Which red blood cells are P. falciparum-infected, and which are of indeterminate infection status?
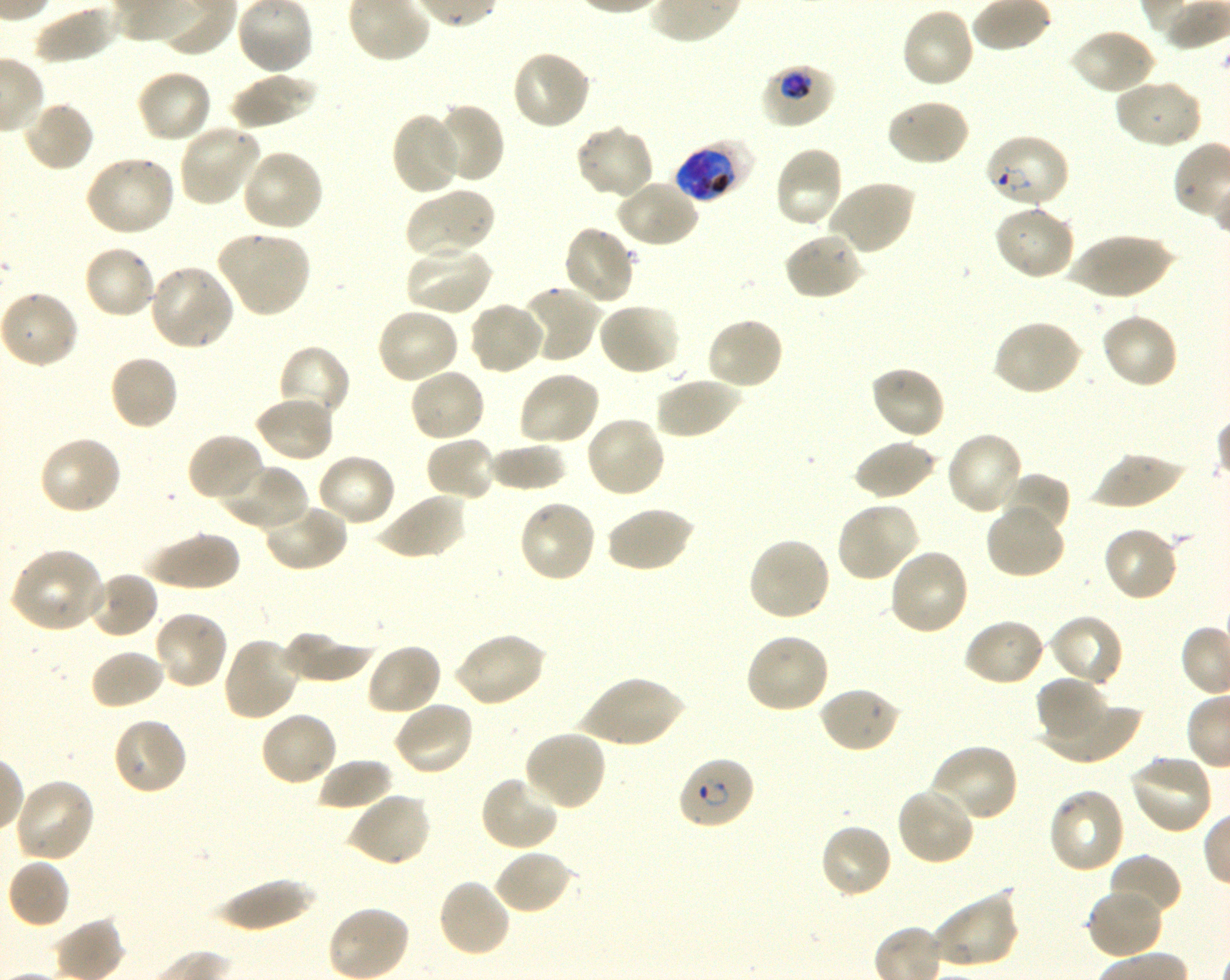
Approximate bounding boxes as [x1, y1, x2, y2] in pixels. Not every red blood cell is marked. A life-cycle stage — or a range of stages, where the recorded stages span more than one — follows each staged infected red blood cell.
Infected red blood cells: [760, 63, 837, 128] trophozoite; [984, 133, 1071, 210] ring; [675, 139, 755, 203] early trophozoite to early schizont; [678, 756, 756, 830] ring.
No red blood cells of indeterminate infection status observed.

Summary:
  - Locations of uninfected red blood cells: [33, 2, 117, 64], [900, 6, 975, 90], [1069, 27, 1157, 97], [510, 50, 593, 131], [136, 68, 214, 144], [227, 72, 319, 129], [1112, 77, 1203, 149], [885, 97, 970, 168], [22, 99, 95, 174], [429, 103, 505, 185], [391, 111, 464, 196], [177, 123, 263, 207], [575, 125, 654, 200], [773, 147, 844, 229], [240, 149, 325, 233], [85, 154, 177, 237], [615, 178, 700, 249], [826, 180, 915, 256], [403, 189, 494, 259], [993, 203, 1075, 281], [562, 224, 636, 307], [215, 230, 311, 318], [782, 230, 864, 301], [1063, 233, 1176, 300], [83, 244, 158, 319], [404, 244, 493, 317], [147, 263, 236, 351], [518, 285, 602, 364], [1, 290, 81, 369], [466, 300, 546, 376], [597, 301, 681, 376], [375, 308, 460, 385], [1100, 311, 1181, 389], [706, 317, 785, 392], [992, 318, 1083, 397], [277, 344, 352, 422], [108, 353, 179, 432], [868, 365, 946, 441], [407, 367, 487, 444], [517, 369, 601, 446], [655, 375, 743, 440], [253, 396, 335, 464], [584, 415, 667, 498], [945, 431, 1025, 517], [186, 432, 265, 504], [38, 434, 123, 515], [424, 435, 498, 503], [854, 439, 937, 501], [488, 441, 567, 492], [315, 452, 397, 528], [1089, 452, 1185, 509], [217, 461, 309, 532], [1000, 471, 1072, 535], [375, 493, 467, 561], [517, 498, 598, 584], [836, 501, 920, 583], [985, 501, 1066, 581], [261, 502, 348, 573], [605, 505, 695, 574], [1102, 525, 1181, 602], [142, 530, 242, 591], [746, 537, 831, 622], [888, 547, 971, 636], [8, 548, 110, 634], [88, 570, 160, 639], [153, 609, 231, 691], [1048, 613, 1125, 689], [962, 617, 1045, 687], [278, 629, 375, 683], [452, 631, 548, 708], [744, 632, 831, 714], [222, 636, 301, 722], [364, 642, 443, 717], [88, 648, 166, 711], [576, 676, 688, 747], [1036, 676, 1109, 742], [817, 685, 902, 754], [1045, 700, 1140, 765], [391, 701, 475, 777], [259, 710, 338, 787], [111, 716, 188, 797], [522, 729, 607, 811], [928, 743, 1019, 824], [1129, 753, 1215, 835], [317, 757, 394, 811], [479, 774, 560, 853], [13, 777, 95, 863], [896, 786, 976, 866], [1048, 786, 1126, 874], [348, 790, 433, 867], [818, 822, 894, 900], [493, 849, 575, 916], [1108, 854, 1181, 922], [6, 858, 70, 929], [209, 876, 317, 932], [436, 878, 513, 959], [1086, 887, 1164, 960], [931, 889, 1019, 970]
  - Life-cycle stages observed: ring, trophozoite
  - Culture: P. falciparum strain 3D7, shaking, in vitro
  - Objective: 100x, oil immersion, numerical aperture 1.30
  - Field of view: one from this slide
  - Preparation: thin blood film
  - Stain: Giemsa
  - Donor blood group: O+
  - Image size: 1230×980 pixels